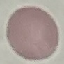

result = no malaria parasites seen
capture = smartphone camera at the microscope eyepiece
preparation = thin blood smear
image type = automatically extracted cell patch, resized to 64 × 64 pixels
stain = Giemsa